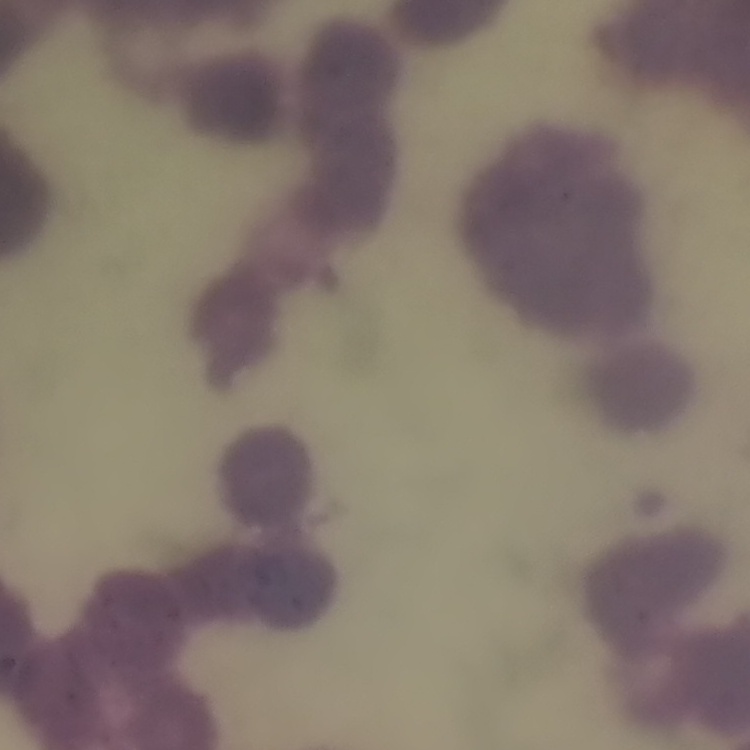

The erythrocytes show rouleaux formation. Thin peripheral smear. Stained with either Field's or Giemsa. One tile cut from a larger photomicrograph.